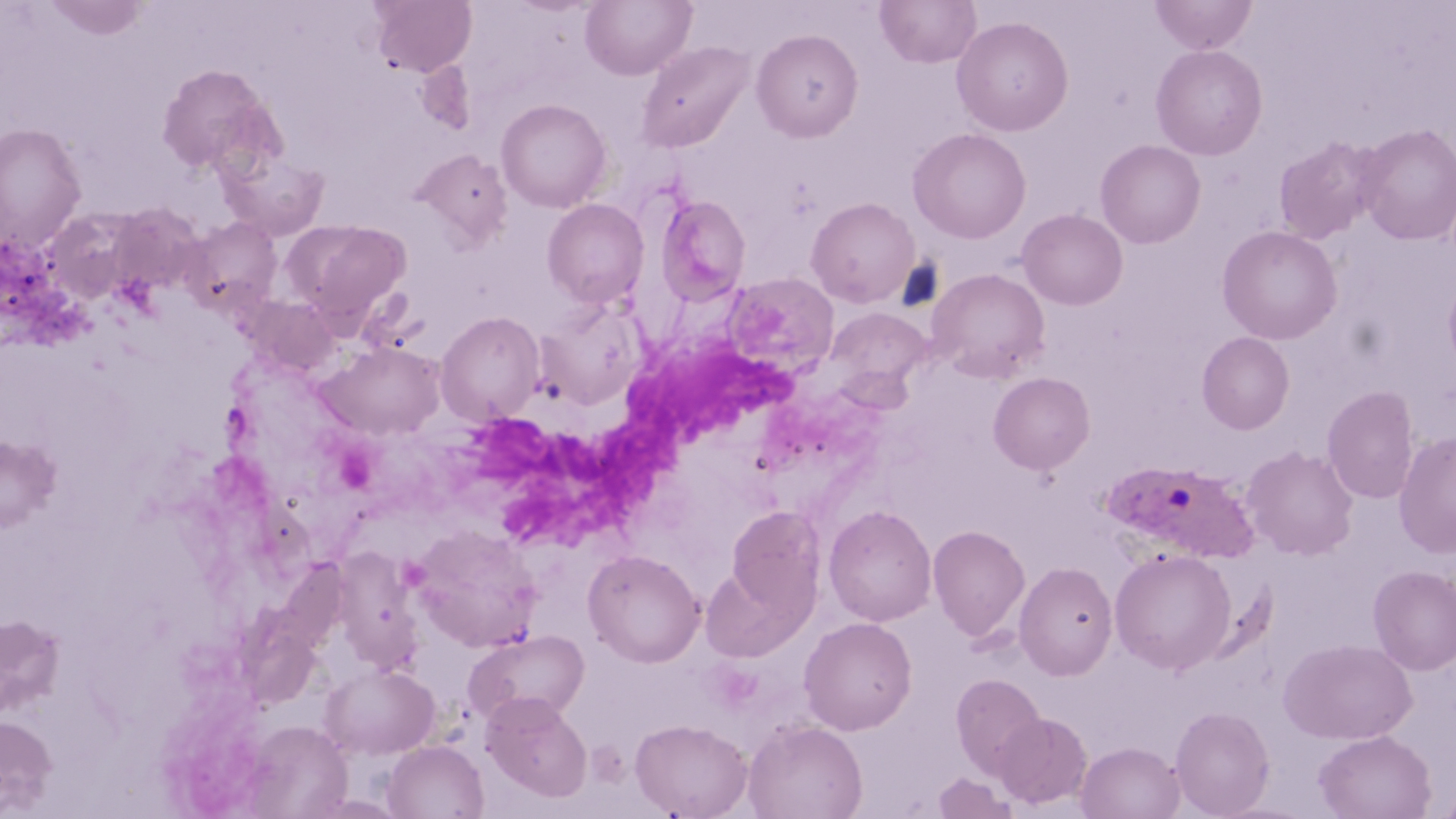

Approximate bounding boxes as named x1/y1/x2/y2 corners in pixels. Uninfected red blood cell locations: (x1=44, y1=0, x2=147, y2=40), (x1=369, y1=0, x2=477, y2=77), (x1=580, y1=0, x2=697, y2=80), (x1=875, y1=0, x2=982, y2=68), (x1=1150, y1=0, x2=1258, y2=54), (x1=952, y1=16, x2=1074, y2=136), (x1=751, y1=28, x2=863, y2=142), (x1=636, y1=40, x2=754, y2=153), (x1=1151, y1=44, x2=1268, y2=160), (x1=416, y1=59, x2=477, y2=134), (x1=155, y1=63, x2=281, y2=177), (x1=496, y1=98, x2=611, y2=213), (x1=0, y1=122, x2=87, y2=253), (x1=1356, y1=123, x2=1456, y2=245), (x1=908, y1=127, x2=1031, y2=244), (x1=1273, y1=136, x2=1384, y2=244), (x1=1095, y1=139, x2=1206, y2=248), (x1=410, y1=148, x2=512, y2=249), (x1=219, y1=149, x2=330, y2=241), (x1=656, y1=193, x2=751, y2=304), (x1=806, y1=197, x2=919, y2=308), (x1=543, y1=198, x2=650, y2=307), (x1=109, y1=203, x2=203, y2=293), (x1=42, y1=208, x2=143, y2=303), (x1=1017, y1=209, x2=1128, y2=310), (x1=180, y1=216, x2=282, y2=317), (x1=289, y1=220, x2=411, y2=326), (x1=1216, y1=225, x2=1343, y2=345), (x1=928, y1=268, x2=1050, y2=382), (x1=724, y1=273, x2=838, y2=374), (x1=1443, y1=276, x2=1456, y2=374), (x1=243, y1=295, x2=341, y2=376), (x1=827, y1=308, x2=933, y2=394), (x1=436, y1=311, x2=544, y2=425), (x1=1197, y1=332, x2=1295, y2=434), (x1=318, y1=342, x2=446, y2=440), (x1=988, y1=372, x2=1095, y2=474), (x1=1322, y1=385, x2=1420, y2=504), (x1=1394, y1=431, x2=1456, y2=559), (x1=0, y1=435, x2=60, y2=532), (x1=1241, y1=445, x2=1359, y2=560), (x1=725, y1=505, x2=825, y2=621), (x1=824, y1=505, x2=937, y2=626), (x1=409, y1=524, x2=544, y2=651), (x1=928, y1=525, x2=1030, y2=642), (x1=1109, y1=548, x2=1236, y2=674), (x1=583, y1=549, x2=705, y2=667), (x1=1014, y1=561, x2=1118, y2=681), (x1=699, y1=563, x2=812, y2=663), (x1=1368, y1=565, x2=1456, y2=674), (x1=0, y1=613, x2=65, y2=719), (x1=799, y1=616, x2=917, y2=735), (x1=464, y1=628, x2=590, y2=727), (x1=1280, y1=638, x2=1416, y2=744), (x1=320, y1=663, x2=439, y2=758), (x1=951, y1=674, x2=1046, y2=777), (x1=481, y1=691, x2=592, y2=801), (x1=1170, y1=706, x2=1275, y2=818), (x1=994, y1=712, x2=1093, y2=810), (x1=0, y1=715, x2=57, y2=814), (x1=630, y1=718, x2=752, y2=819), (x1=743, y1=718, x2=868, y2=819), (x1=242, y1=719, x2=352, y2=817), (x1=1313, y1=730, x2=1436, y2=818), (x1=382, y1=740, x2=488, y2=819), (x1=1076, y1=741, x2=1185, y2=819), (x1=932, y1=771, x2=1018, y2=819), (x1=1435, y1=787, x2=1456, y2=818). Plasmodium ovale-infected red blood cell locations: (x1=1102, y1=461, x2=1260, y2=563). White blood cell locations: (x1=483, y1=342, x2=806, y2=554). Slide-level diagnosis: Plasmodium ovale. Image is 1456×819 pixels. One field of a larger specimen. Thin blood film. May-Grünwald-Giemsa-stained preparation. Captured at 1000x magnification. Light microscopy.